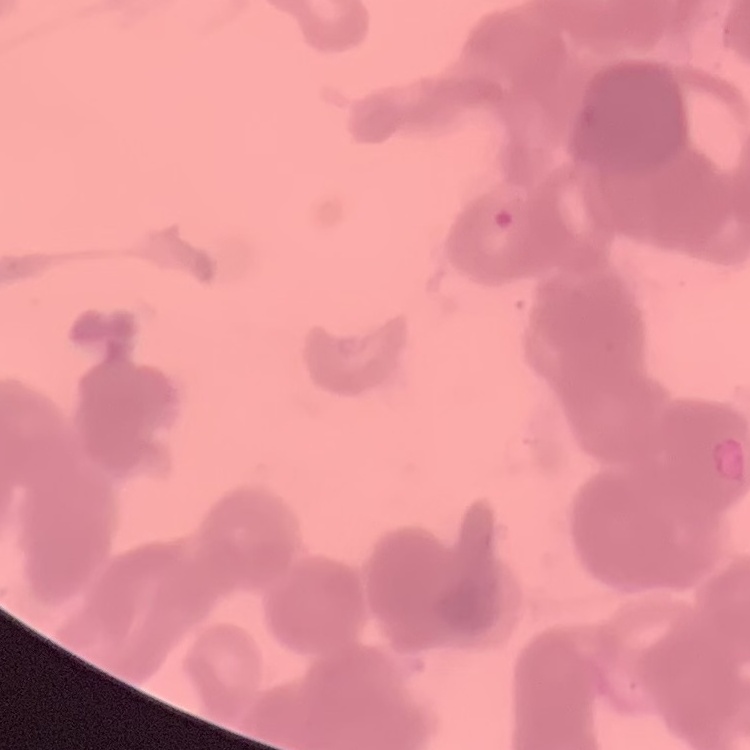 The red blood cells exhibit rouleaux formation. Square crop of a larger photomicrograph. Thin blood film. Field's or Giemsa stain.